Evaluate for Plasmodium parasites.
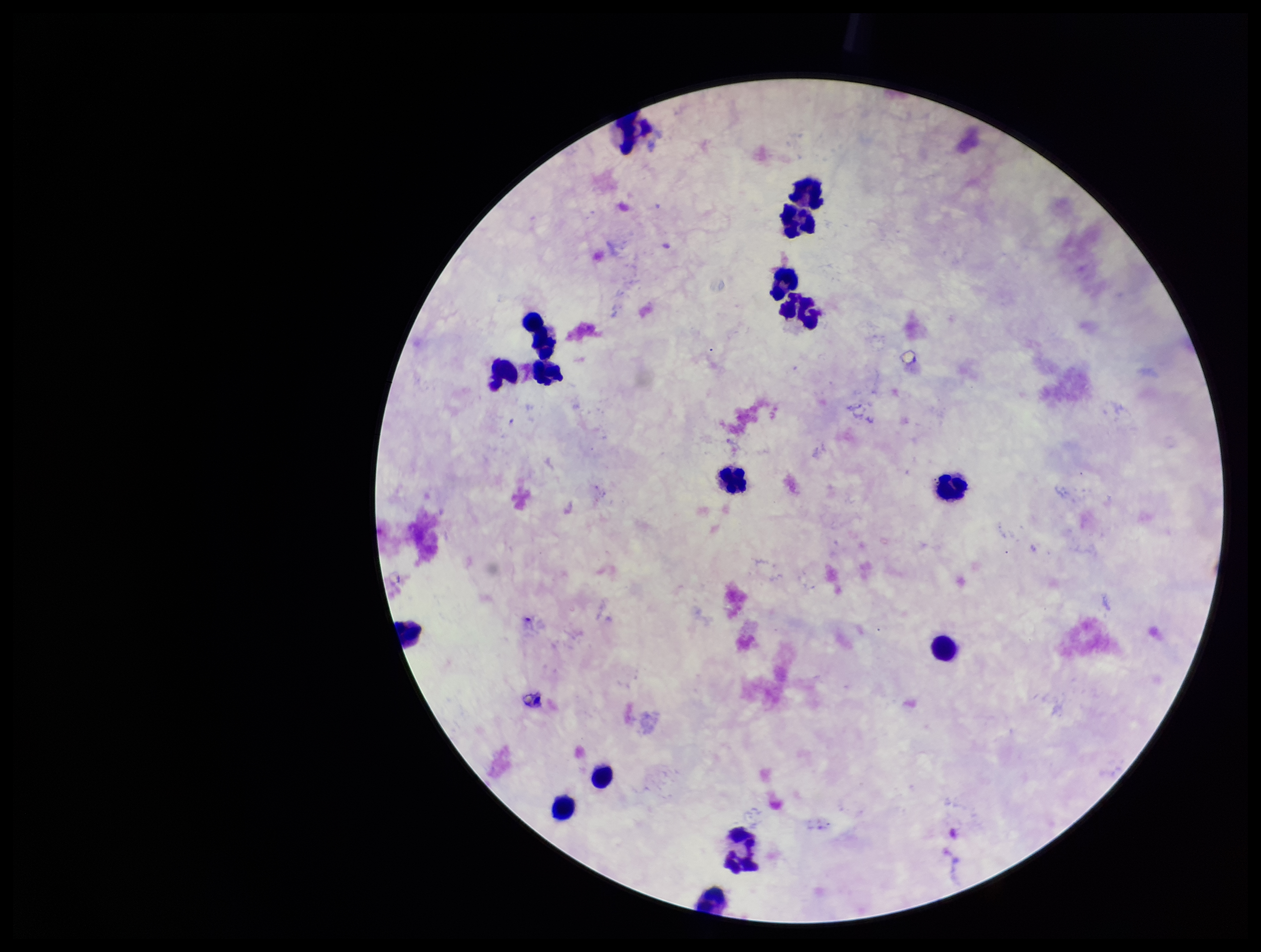

None seen.

Summary:
  - Parasite count: 0
  - Leukocyte count: 14
  - Capture: smartphone photograph through the microscope eyepiece
  - Stain: Giemsa
  - Patient malaria status: negative
  - Image size: 1261×952 pixels
  - Field of view: single
  - Preparation: thick smear